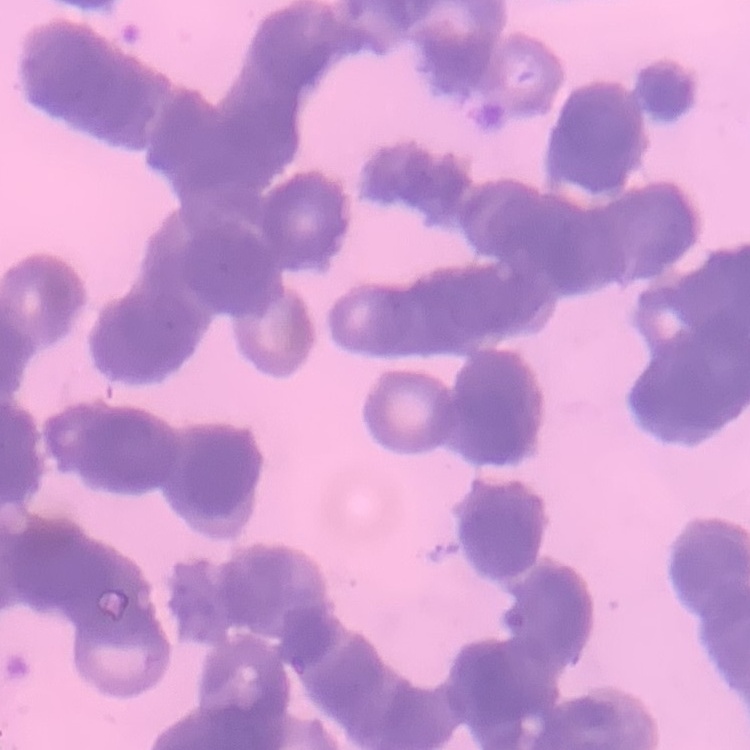

Summary:
  - Erythrocyte morphology: rouleaux formation
  - Preparation: thin blood smear
  - Stain: Field's or Giemsa
  - Image type: square crop of a larger photomicrograph